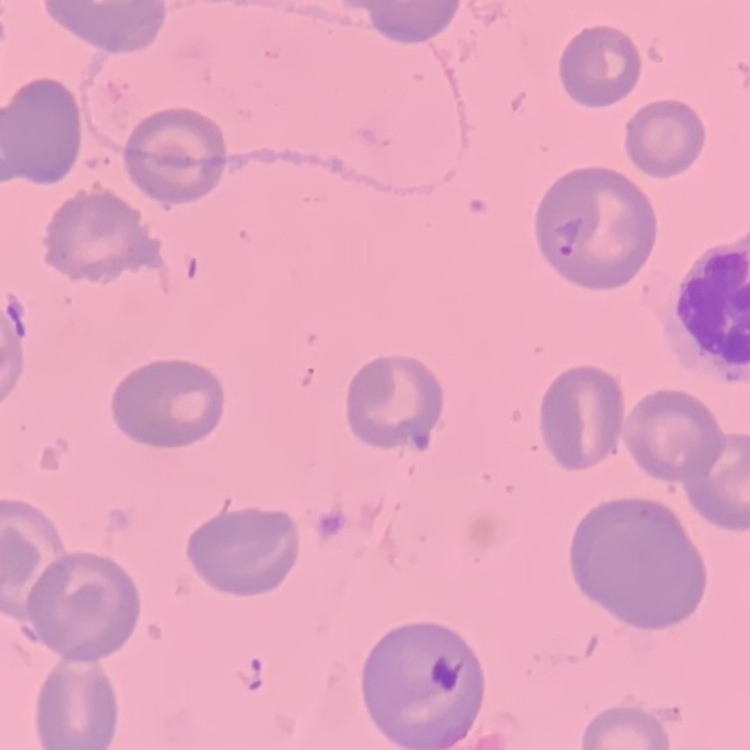
red blood cell morphology = no rouleaux formation
stain = Field's or Giemsa
image type = square crop of a larger photomicrograph
preparation = thin peripheral smear